Outline each blood parasite and name the species.
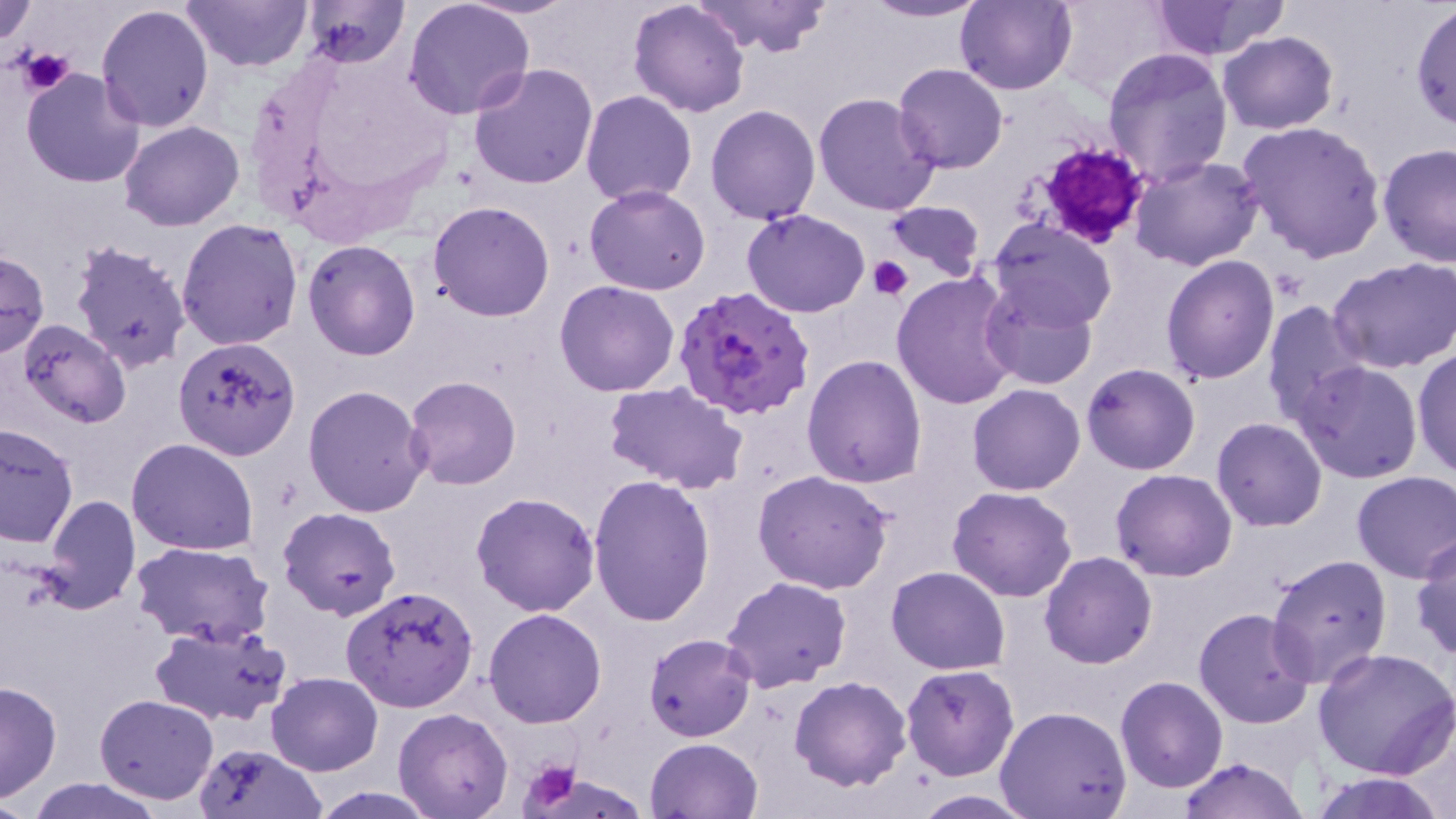

Approximate bounding boxes as named x1/y1/x2/y2 corners in pixels.
Plasmodium falciparum-infected red blood cells: (x1=673, y1=286, x2=816, y2=421).
No Plasmodium ovale, Plasmodium malariae, Plasmodium vivax, Babesia divergens, or Trypanosoma brucei observed.

Summary:
  - Uninfected red blood cell locations: (x1=1, y1=0, x2=37, y2=48), (x1=183, y1=0, x2=313, y2=72), (x1=299, y1=0, x2=409, y2=69), (x1=464, y1=0, x2=578, y2=20), (x1=859, y1=0, x2=991, y2=23), (x1=1049, y1=0, x2=1172, y2=102), (x1=1148, y1=0, x2=1279, y2=59), (x1=403, y1=1, x2=536, y2=121), (x1=690, y1=1, x2=834, y2=59), (x1=954, y1=1, x2=1075, y2=95), (x1=1409, y1=1, x2=1456, y2=132), (x1=627, y1=2, x2=750, y2=117), (x1=95, y1=5, x2=215, y2=132), (x1=1218, y1=31, x2=1339, y2=134), (x1=1102, y1=46, x2=1234, y2=186), (x1=468, y1=61, x2=599, y2=189), (x1=893, y1=62, x2=1010, y2=174), (x1=21, y1=70, x2=147, y2=187), (x1=580, y1=90, x2=699, y2=206), (x1=811, y1=91, x2=941, y2=217), (x1=705, y1=104, x2=820, y2=223), (x1=1235, y1=119, x2=1387, y2=263), (x1=119, y1=120, x2=245, y2=232), (x1=1378, y1=143, x2=1456, y2=269), (x1=1129, y1=155, x2=1265, y2=273), (x1=585, y1=185, x2=712, y2=295), (x1=427, y1=201, x2=554, y2=322), (x1=880, y1=202, x2=986, y2=282), (x1=742, y1=208, x2=871, y2=317), (x1=988, y1=218, x2=1116, y2=331), (x1=176, y1=219, x2=304, y2=352), (x1=67, y1=237, x2=194, y2=374), (x1=302, y1=239, x2=421, y2=361), (x1=0, y1=250, x2=48, y2=357), (x1=1160, y1=255, x2=1281, y2=386), (x1=1328, y1=255, x2=1456, y2=373), (x1=891, y1=271, x2=1023, y2=412), (x1=979, y1=279, x2=1099, y2=391), (x1=553, y1=280, x2=681, y2=398), (x1=1262, y1=300, x2=1372, y2=428), (x1=15, y1=319, x2=132, y2=430), (x1=174, y1=338, x2=300, y2=459), (x1=1411, y1=343, x2=1456, y2=480), (x1=802, y1=355, x2=928, y2=488), (x1=1293, y1=361, x2=1424, y2=483), (x1=1082, y1=362, x2=1200, y2=475), (x1=404, y1=376, x2=522, y2=490), (x1=604, y1=381, x2=749, y2=493), (x1=967, y1=382, x2=1086, y2=495), (x1=302, y1=384, x2=431, y2=518), (x1=1211, y1=417, x2=1327, y2=532), (x1=0, y1=422, x2=78, y2=547), (x1=126, y1=438, x2=258, y2=555), (x1=753, y1=469, x2=896, y2=595), (x1=1112, y1=469, x2=1237, y2=581), (x1=1351, y1=470, x2=1456, y2=582), (x1=585, y1=475, x2=716, y2=624), (x1=947, y1=486, x2=1078, y2=603), (x1=470, y1=491, x2=600, y2=617), (x1=39, y1=494, x2=141, y2=615), (x1=277, y1=506, x2=401, y2=622), (x1=1410, y1=534, x2=1456, y2=663), (x1=131, y1=541, x2=273, y2=644), (x1=1040, y1=552, x2=1157, y2=669), (x1=1265, y1=552, x2=1394, y2=688), (x1=886, y1=567, x2=1011, y2=675), (x1=722, y1=576, x2=852, y2=690), (x1=340, y1=586, x2=479, y2=713), (x1=482, y1=607, x2=608, y2=729), (x1=1193, y1=607, x2=1316, y2=728), (x1=149, y1=622, x2=292, y2=727), (x1=645, y1=634, x2=756, y2=741), (x1=1313, y1=647, x2=1456, y2=780), (x1=902, y1=664, x2=1019, y2=780), (x1=265, y1=671, x2=382, y2=775), (x1=788, y1=675, x2=912, y2=790), (x1=1116, y1=675, x2=1228, y2=792), (x1=0, y1=681, x2=63, y2=802), (x1=93, y1=693, x2=219, y2=805), (x1=994, y1=705, x2=1132, y2=819), (x1=393, y1=708, x2=512, y2=819), (x1=645, y1=737, x2=764, y2=819), (x1=190, y1=742, x2=327, y2=819), (x1=1176, y1=756, x2=1310, y2=818), (x1=1309, y1=770, x2=1447, y2=819), (x1=23, y1=777, x2=167, y2=819), (x1=910, y1=792, x2=1039, y2=818)
  - Platelet locations: (x1=20, y1=49, x2=75, y2=95), (x1=1029, y1=141, x2=1152, y2=249), (x1=868, y1=256, x2=912, y2=300), (x1=521, y1=757, x2=585, y2=814)
  - Slide-level diagnosis: Plasmodium falciparum
  - Modality: optical microscopy
  - Image size: 1456×819 pixels
  - Stain: May-Grünwald-Giemsa
  - Field of view: one of a larger specimen
  - Magnification: 1000x
  - Preparation: thin blood film